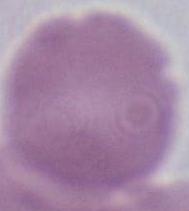

identification = red blood cell
magnification = 1000x
modality = micrograph